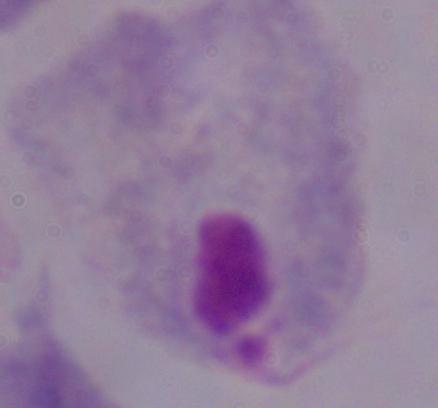 1000x magnification. Micrograph. A trichomonad is seen.